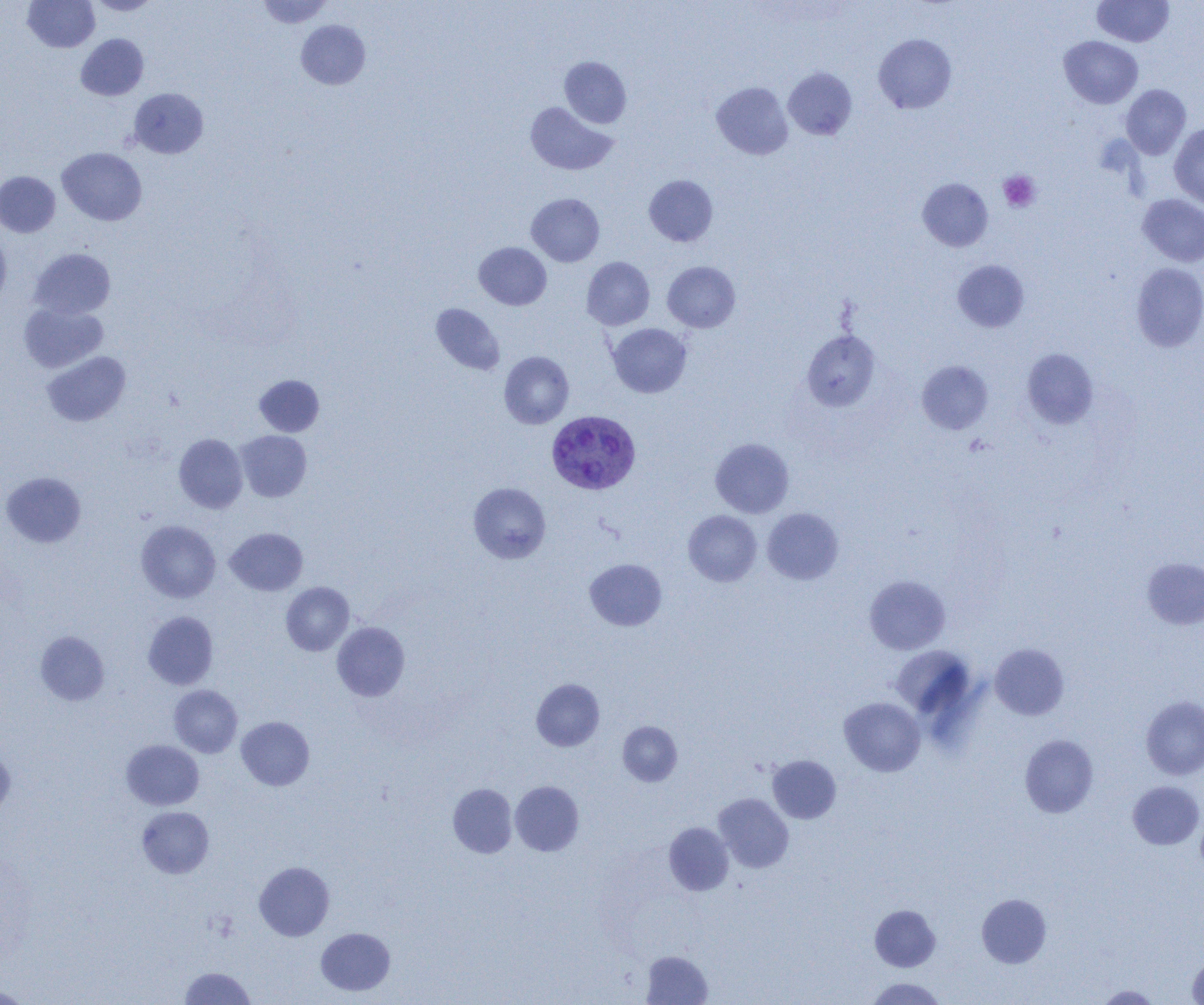

{
  "slide_level_diagnosis": "Plasmodium vivax",
  "image_size": "1204×1005 pixels",
  "field_of_view": "single",
  "modality": "optical microscopy",
  "platelet_locations": "approximate bounding boxes as named x1/y1/x2/y2 corners in pixels: (x1=998, y1=171, x2=1041, y2=212)",
  "uninfected_red_blood_cell_locations": "approximate bounding boxes as named x1/y1/x2/y2 corners in pixels: (x1=23, y1=0, x2=100, y2=52), (x1=257, y1=0, x2=333, y2=28), (x1=1092, y1=0, x2=1174, y2=47), (x1=86, y1=1, x2=161, y2=16), (x1=296, y1=20, x2=370, y2=90), (x1=76, y1=34, x2=148, y2=100), (x1=873, y1=34, x2=957, y2=114), (x1=1059, y1=35, x2=1143, y2=108), (x1=560, y1=56, x2=631, y2=128), (x1=783, y1=67, x2=857, y2=140), (x1=711, y1=82, x2=793, y2=159), (x1=1121, y1=84, x2=1191, y2=159), (x1=129, y1=88, x2=208, y2=158), (x1=525, y1=102, x2=618, y2=175), (x1=1169, y1=123, x2=1204, y2=209), (x1=57, y1=147, x2=147, y2=225), (x1=0, y1=171, x2=60, y2=237), (x1=644, y1=175, x2=718, y2=246), (x1=917, y1=178, x2=993, y2=251), (x1=526, y1=193, x2=604, y2=266), (x1=1137, y1=194, x2=1204, y2=267), (x1=0, y1=231, x2=11, y2=307), (x1=474, y1=242, x2=551, y2=309), (x1=29, y1=247, x2=116, y2=319), (x1=582, y1=257, x2=655, y2=330), (x1=953, y1=260, x2=1029, y2=332), (x1=662, y1=261, x2=740, y2=332), (x1=1131, y1=263, x2=1204, y2=352), (x1=19, y1=302, x2=107, y2=372), (x1=431, y1=303, x2=505, y2=375), (x1=607, y1=323, x2=691, y2=398), (x1=802, y1=329, x2=880, y2=411), (x1=1021, y1=348, x2=1099, y2=429), (x1=42, y1=351, x2=130, y2=426), (x1=499, y1=351, x2=574, y2=428), (x1=916, y1=361, x2=993, y2=434), (x1=254, y1=375, x2=324, y2=436), (x1=235, y1=430, x2=311, y2=502), (x1=174, y1=433, x2=247, y2=513), (x1=710, y1=438, x2=794, y2=518), (x1=1, y1=472, x2=86, y2=548), (x1=469, y1=482, x2=551, y2=563), (x1=762, y1=508, x2=844, y2=584), (x1=683, y1=510, x2=762, y2=586), (x1=136, y1=520, x2=220, y2=603), (x1=225, y1=527, x2=307, y2=595), (x1=1142, y1=557, x2=1204, y2=629), (x1=585, y1=559, x2=666, y2=630), (x1=864, y1=575, x2=950, y2=655), (x1=281, y1=582, x2=354, y2=655), (x1=143, y1=611, x2=218, y2=689), (x1=332, y1=622, x2=409, y2=701), (x1=36, y1=631, x2=109, y2=705), (x1=990, y1=643, x2=1069, y2=720), (x1=891, y1=646, x2=976, y2=718), (x1=531, y1=679, x2=604, y2=751), (x1=169, y1=685, x2=242, y2=758), (x1=1140, y1=696, x2=1204, y2=780), (x1=839, y1=697, x2=925, y2=776), (x1=236, y1=716, x2=314, y2=790), (x1=618, y1=721, x2=682, y2=786), (x1=1019, y1=734, x2=1099, y2=817), (x1=121, y1=740, x2=204, y2=810), (x1=0, y1=747, x2=15, y2=818), (x1=768, y1=755, x2=841, y2=823), (x1=510, y1=781, x2=584, y2=856), (x1=1128, y1=781, x2=1204, y2=850), (x1=448, y1=783, x2=517, y2=858), (x1=714, y1=793, x2=793, y2=872), (x1=137, y1=806, x2=214, y2=878), (x1=664, y1=822, x2=734, y2=896), (x1=254, y1=861, x2=334, y2=941), (x1=976, y1=893, x2=1052, y2=968), (x1=870, y1=904, x2=941, y2=971), (x1=316, y1=927, x2=395, y2=996), (x1=641, y1=951, x2=713, y2=1004), (x1=1187, y1=956, x2=1204, y2=1004), (x1=180, y1=967, x2=255, y2=1004), (x1=866, y1=977, x2=946, y2=1004), (x1=1095, y1=985, x2=1161, y2=1004), (x1=0, y1=986, x2=32, y2=1004)",
  "plasmodium_vivax_infected_red_blood_cell_locations": "approximate bounding boxes as named x1/y1/x2/y2 corners in pixels: (x1=547, y1=411, x2=640, y2=495)",
  "preparation": "thin blood smear",
  "magnification": "1000x"
}